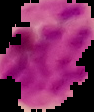

malaria status = parasitized
preparation = thin blood smear
image type = cell region segmented out of the field of view; surrounding area masked to black
image size = 94×112 pixels